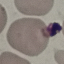
result: no malaria parasites seen
stain: Giemsa
capture: smartphone through the microscope eyepiece
image_type: automatically extracted cell patch, resized to 64 × 64 pixels
preparation: thin smear